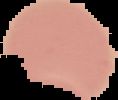
Summary:
  - Result: no malaria parasites detected
  - Image type: segmented cell region on a black background
  - Image size: 118×100 pixels
  - Preparation: thin blood film